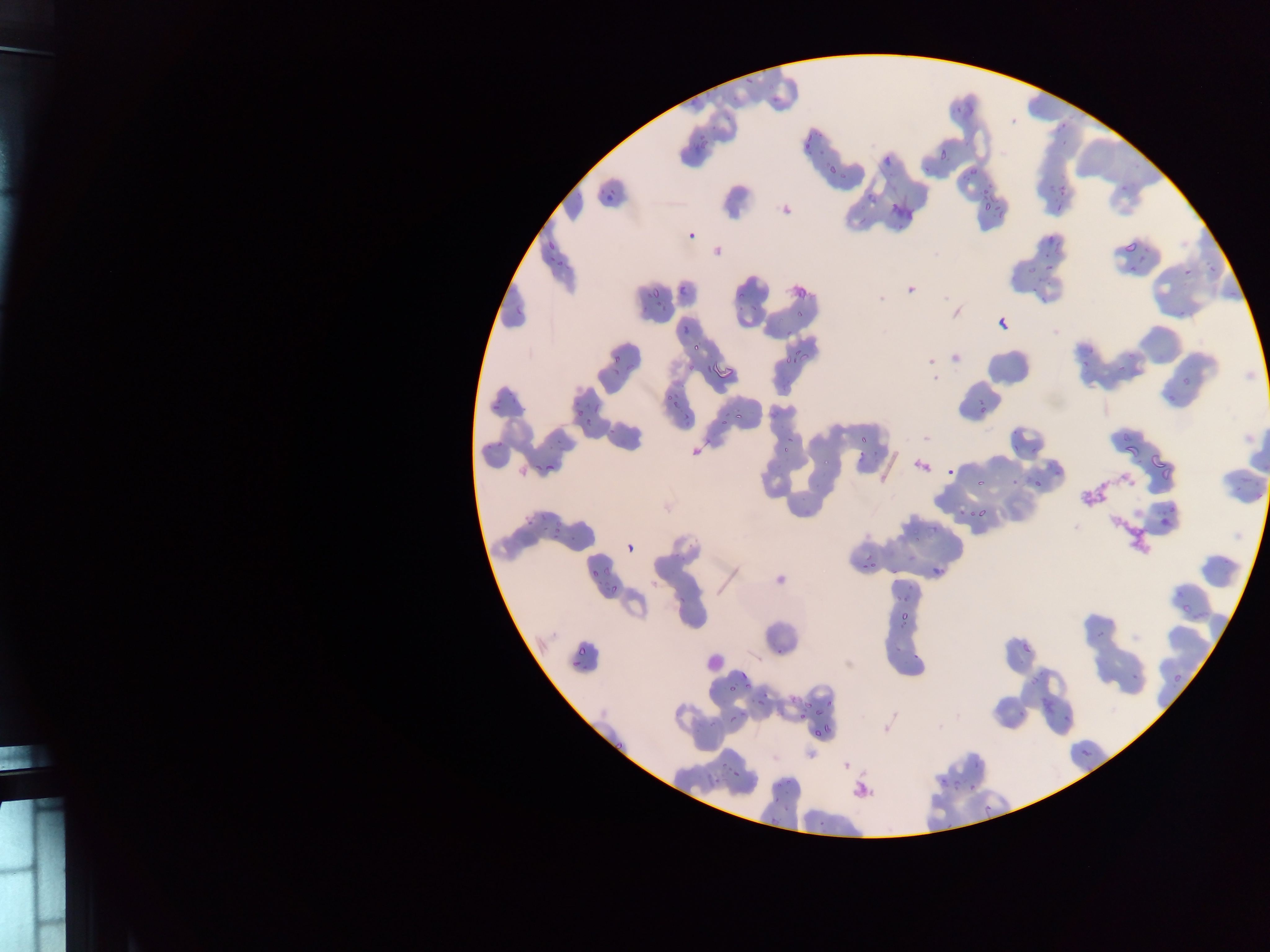

{
  "capture": "mobile-phone photograph through a microscope",
  "preparation": "thin blood film",
  "field_of_view": "single",
  "country": "Ghana",
  "malaria_parasite_locations": "approximate bounding boxes as left top right bottom in pixels: 802 132 815 151; 688 142 705 160; 932 147 951 163; 881 155 897 165; 825 161 841 177; 965 166 976 175; 980 176 991 197; 1048 182 1056 198; 604 184 617 202; 1117 184 1134 195; 1060 186 1074 196; 865 193 882 206; 974 197 991 214; 995 208 1004 221; 686 228 696 239; 1043 229 1058 247; 545 236 554 251; 1122 241 1137 256; 548 251 565 266; 1138 255 1148 264; 1025 258 1038 278; 1043 258 1055 278; 1126 264 1138 275; 1180 264 1193 278; 1208 264 1217 277; 650 280 664 296; 678 280 689 291; 736 284 750 297; 792 285 809 298; 1029 285 1042 298; 655 298 671 311; 514 299 529 317; 736 301 746 313; 992 304 1010 331; 680 317 697 331; 689 338 700 355; 787 346 806 367; 609 350 620 368; 688 359 695 372; 704 362 712 375; 715 364 737 385; 1176 375 1193 392; 660 387 675 407; 979 387 988 420; 488 397 501 412; 572 400 583 414; 731 402 751 422; 717 411 724 428; 584 414 594 430; 493 429 510 449; 783 432 797 448; 856 434 873 451; 1123 442 1138 458; 530 451 558 473; 1151 456 1172 478; 945 467 954 478; 1032 476 1045 489; 974 477 987 489; 967 504 986 522; 1165 506 1176 516; 525 509 536 526; 547 516 566 541; 1158 518 1170 530; 927 528 939 537; 626 544 632 552; 856 557 880 574; 929 561 942 579; 590 562 603 580; 603 581 620 597; 1173 590 1183 599; 897 602 911 624; 775 638 785 653; 890 640 901 654; 1020 640 1037 657; 912 645 925 664; 573 646 591 655; 569 659 579 673; 738 669 754 689; 1128 672 1140 686; 1171 674 1182 689; 1028 677 1037 690; 721 679 734 699; 804 690 825 714; 755 697 764 706; 1016 704 1033 720; 1062 709 1081 724; 726 713 738 726; 799 713 807 724; 822 715 832 732; 812 730 819 740; 608 735 628 752; 1079 744 1096 764; 719 757 729 779; 972 760 984 769; 729 761 742 782; 955 779 966 792; 938 780 947 791; 770 783 786 798; 969 787 979 796; 773 795 793 809; 817 814 829 828; 759 815 775 835 | approximate x y pixel centers of objects too small to bound: 797 317",
  "image_size": "1270×952 pixels"
}